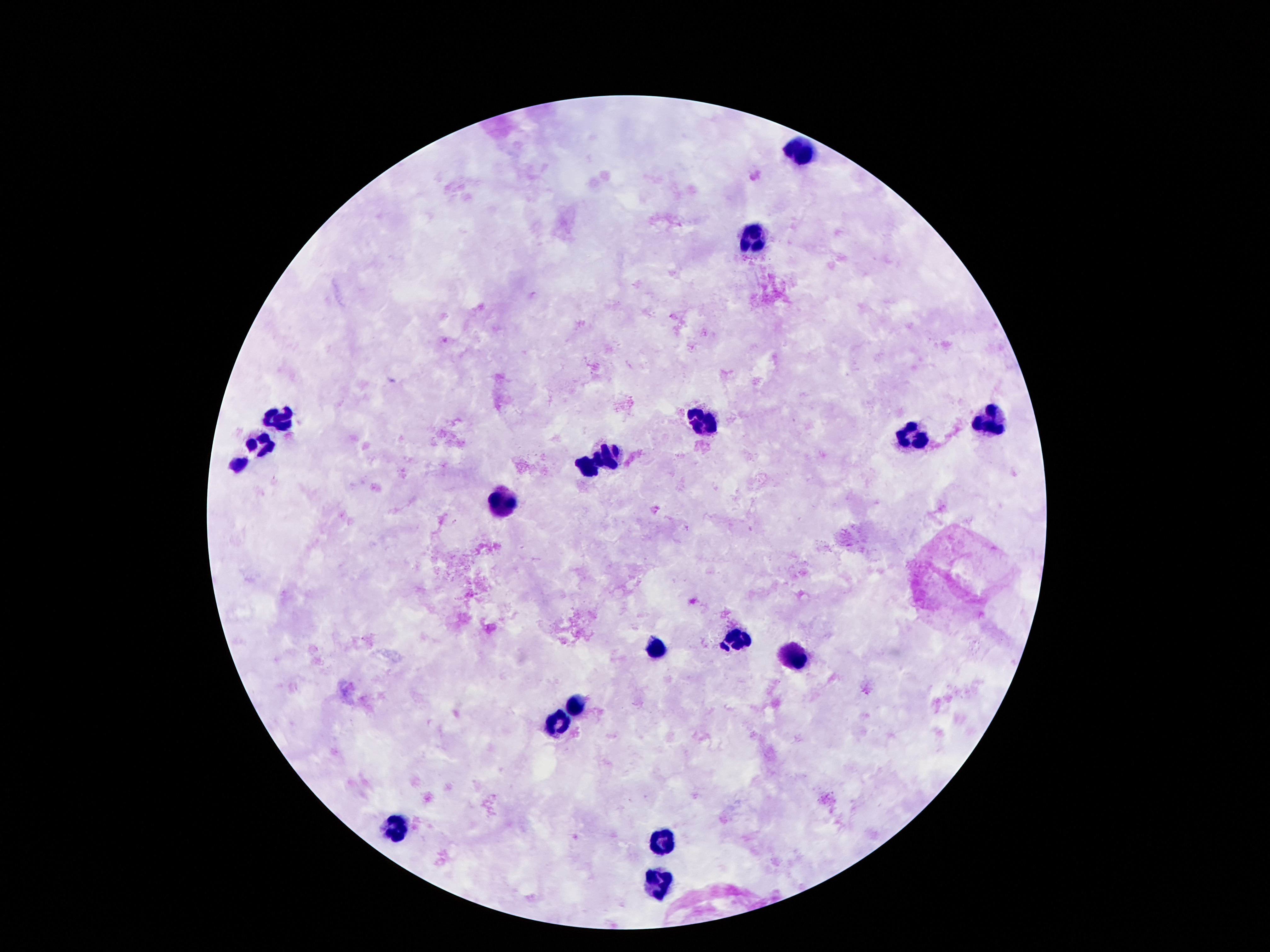
capture = smartphone camera through the microscope eyepiece
preparation = thick blood smear
leukocyte locations = approximate object centers, in pixels from the top-left corner: (x=800, y=151), (x=751, y=240), (x=276, y=418), (x=988, y=418), (x=701, y=426), (x=913, y=434), (x=260, y=447), (x=610, y=453), (x=239, y=464), (x=585, y=467), (x=505, y=502), (x=736, y=640), (x=657, y=649), (x=793, y=658), (x=579, y=703), (x=560, y=726), (x=392, y=830), (x=657, y=844), (x=659, y=886)
field of view = single
image size = 1270×952 pixels
stain = Giemsa
magnification = 100x
patient malaria status = not infected